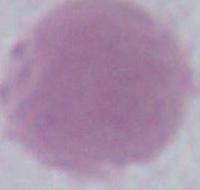

identification = erythrocyte
modality = photomicrograph
magnification = 1000x